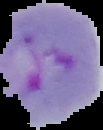

Image is 103×130 pixels. Result: malaria parasites detected. From a thin blood smear. The area outside the segmented cell region is set to black.